Identify the cell.
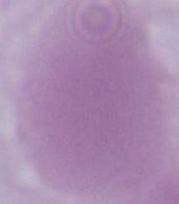

An erythrocyte.

modality = photomicrograph
magnification = 1000x